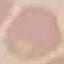 Result: no malaria parasites detected. Giemsa stain. Automatically extracted cell patch, resized to 64 × 64 pixels. Acquired by smartphone through the microscope eyepiece. Thin blood smear.